Point out each Plasmodium parasite.
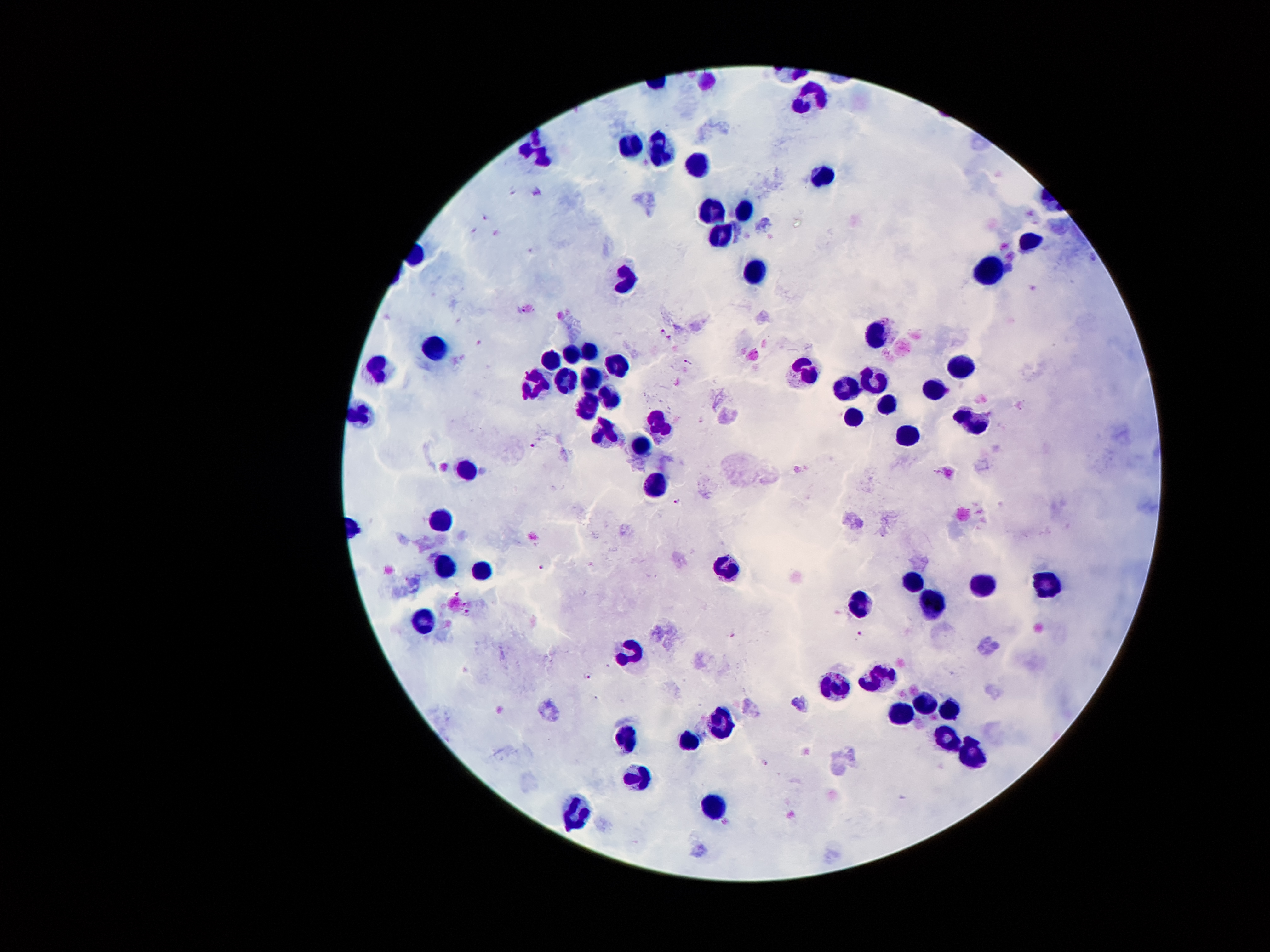
Approximate centers as (x, y) in pixels.
Plasmodium parasites: (511, 190), (538, 191), (485, 218), (474, 232), (664, 331), (670, 338), (478, 342), (689, 363), (532, 445), (678, 502), (541, 569), (456, 593), (465, 603), (467, 613), (732, 633), (860, 633), (588, 676), (765, 763).

patient_malaria_status: infected with Plasmodium falciparum
image_size: 1270×952 pixels
capture: smartphone camera through the microscope eyepiece
preparation: thick blood smear
field_of_view: one from this slide
stain: Giemsa
magnification: 100x
leukocyte_locations: 'approximate centers as (x, y) in pixels: (809, 95), (631, 144), (658, 151), (541, 157), (696, 165), (822, 175), (708, 209), (742, 213), (719, 236), (1028, 240), (990, 270), (755, 273), (623, 282), (875, 332), (437, 350), (587, 350), (571, 354), (555, 358), (614, 361), (386, 369), (961, 371), (809, 372), (590, 374), (569, 378), (874, 381), (536, 382), (850, 388), (934, 389), (610, 396), (886, 403), (589, 407), (972, 416), (853, 421), (663, 427), (609, 435), (910, 436), (643, 447), (469, 471), (654, 485), (444, 518), (444, 566), (725, 567), (478, 569), (915, 582), (1045, 586), (983, 588), (859, 605), (933, 605), (422, 623), (632, 653), (882, 674), (840, 686), (922, 701), (950, 707), (897, 715), (722, 728), (624, 736), (946, 738), (689, 744), (974, 752), (640, 778), (716, 805), (579, 812)'